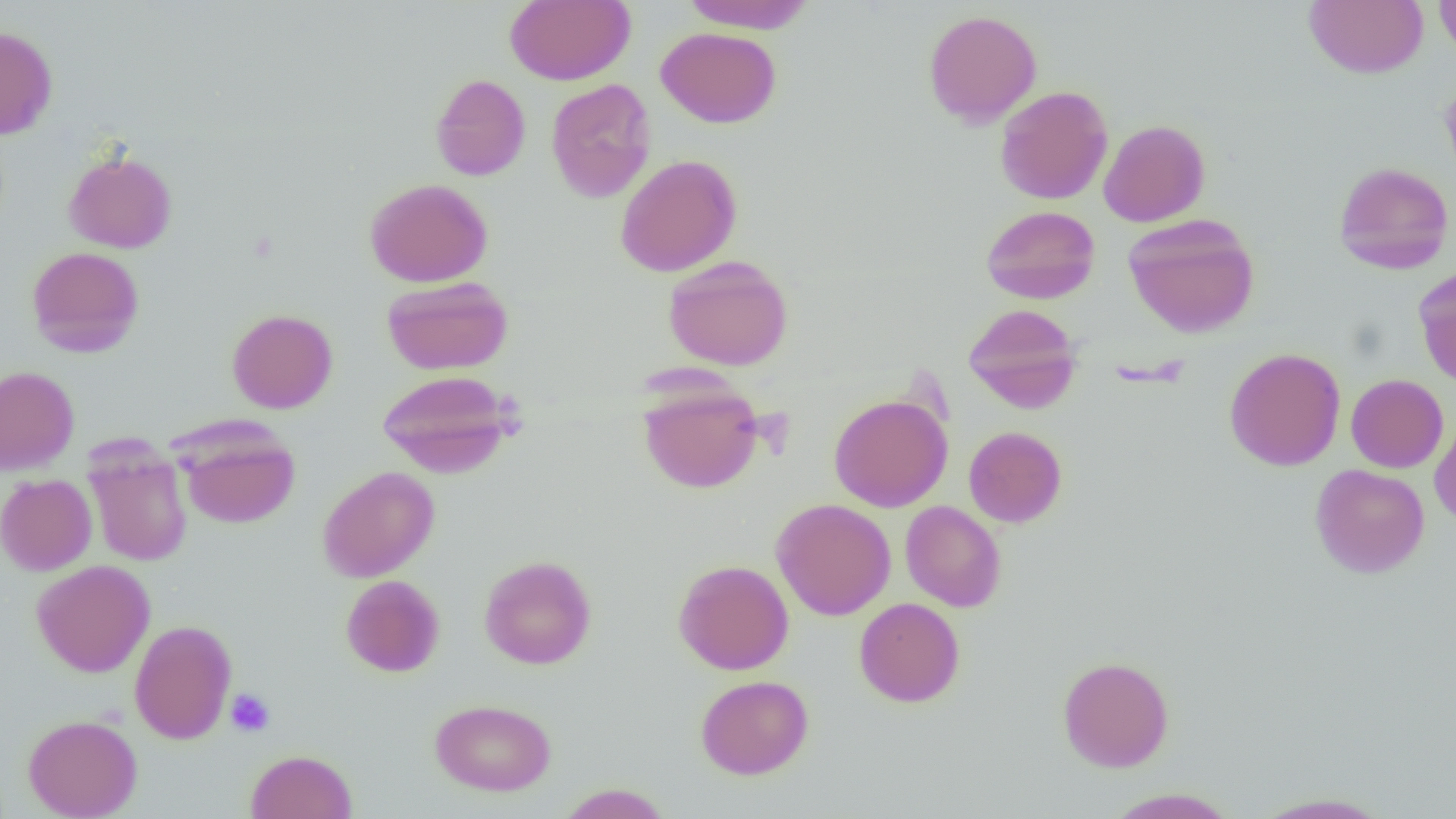
slide-level diagnosis = no evidence of blood parasites
preparation = thin blood smear
magnification = 1000x
modality = light microscopy
uninfected red blood cell locations = approximate bounding boxes as [x1, y1, x2, y2] in pixels: [505, 0, 634, 85], [681, 0, 815, 34], [1303, 0, 1428, 78], [1433, 0, 1456, 59], [922, 9, 1042, 127], [0, 25, 58, 139], [656, 27, 781, 128], [430, 74, 531, 180], [1439, 75, 1456, 193], [545, 78, 656, 203], [995, 85, 1113, 205], [1098, 119, 1210, 227], [62, 149, 178, 254], [615, 154, 742, 277], [1333, 161, 1454, 274], [364, 178, 493, 287], [981, 205, 1101, 304], [1123, 214, 1260, 338], [26, 246, 145, 357], [662, 256, 794, 371], [1414, 266, 1456, 389], [381, 275, 513, 375], [963, 303, 1082, 412], [226, 309, 338, 413], [1224, 347, 1345, 471], [0, 365, 79, 475], [378, 370, 516, 478], [1346, 374, 1448, 473], [638, 381, 763, 494], [828, 393, 953, 512], [1430, 413, 1456, 527], [178, 425, 300, 529], [964, 426, 1067, 527], [85, 444, 192, 567], [1309, 464, 1429, 578], [317, 466, 440, 582], [0, 473, 97, 575], [771, 498, 896, 620], [900, 501, 1006, 612], [479, 555, 597, 669], [30, 559, 155, 677], [672, 559, 794, 675], [340, 575, 445, 677], [854, 597, 965, 707], [129, 619, 237, 744], [1058, 656, 1174, 772], [695, 674, 814, 779], [430, 699, 556, 796], [23, 714, 142, 819], [245, 749, 357, 819], [556, 783, 672, 819], [1103, 788, 1239, 818], [1248, 792, 1396, 818]
image size = 1456×819 pixels
field of view = one of a larger specimen
platelet locations = approximate bounding boxes as [x1, y1, x2, y2] in pixels: [226, 688, 276, 736]